Report the malaria status of this cell.
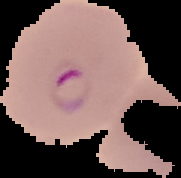
Parasitized.

{
  "image_size": "181×178 pixels",
  "preparation": "thin blood smear",
  "image_type": "cell region segmented out of the field of view; surrounding area masked to black"
}